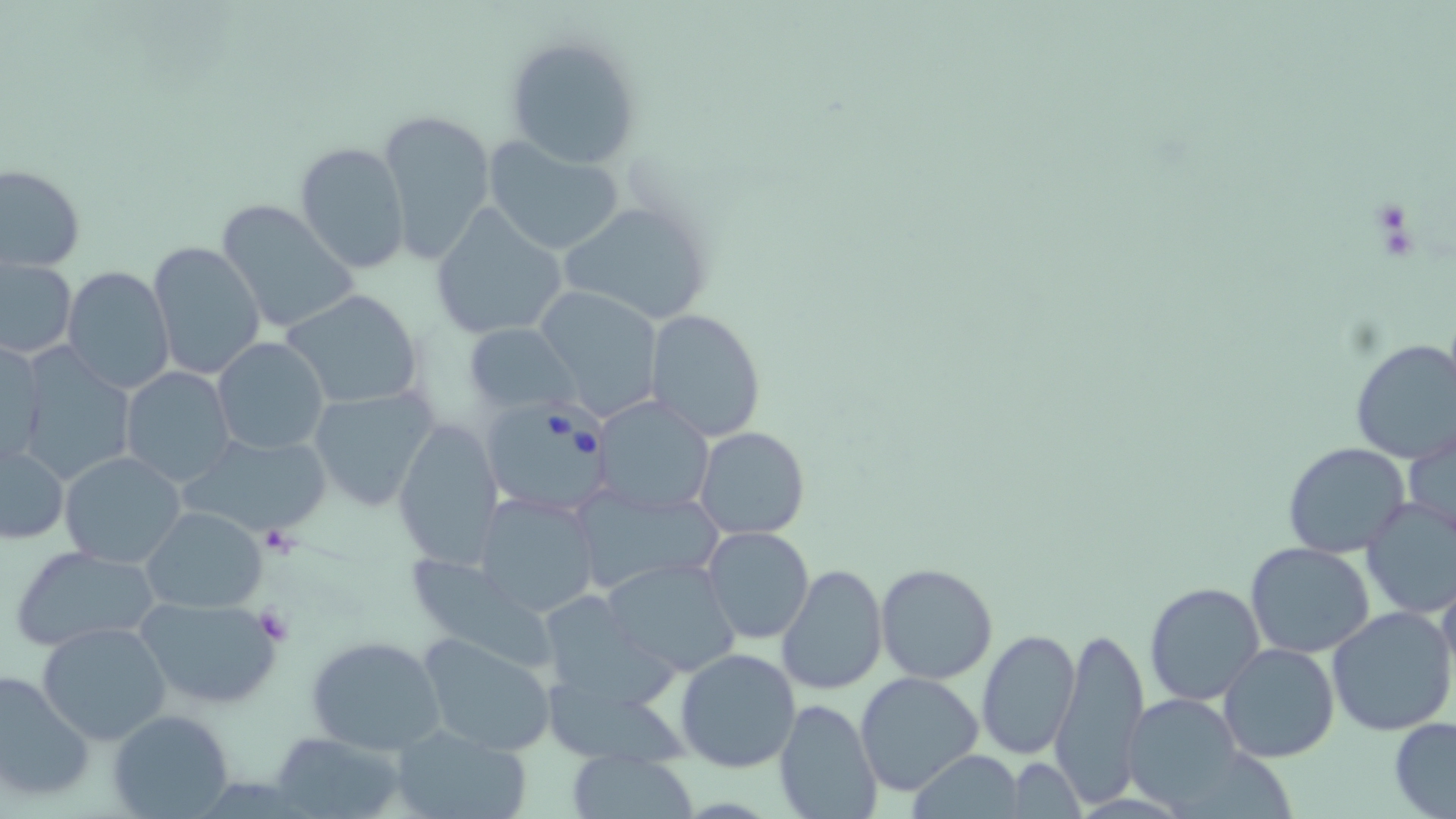 Approximate bounding boxes as (x1,y1)-(x2,y2) corner pairs in pixels. Babesia divergens-infected red blood cell locations: (481,399)-(615,514). Uninfected red blood cell locations: (502,32)-(641,171), (377,107)-(497,267), (483,136)-(626,255), (294,140)-(411,273), (1,164)-(85,272), (215,199)-(358,336), (556,200)-(714,325), (429,206)-(568,341), (148,239)-(266,380), (2,257)-(77,359), (63,266)-(174,392), (531,287)-(662,420), (283,289)-(424,409), (645,308)-(766,441), (463,323)-(579,415), (1349,337)-(1456,464), (212,338)-(330,454), (0,341)-(45,470), (14,352)-(134,486), (120,367)-(235,487), (307,385)-(437,512), (594,396)-(715,515), (393,416)-(503,567), (696,426)-(810,541), (1404,428)-(1456,544), (185,436)-(328,540), (1282,441)-(1410,558), (1,443)-(69,546), (59,451)-(187,568), (569,485)-(721,595), (472,492)-(601,618), (1358,496)-(1456,621), (141,506)-(267,613), (701,527)-(814,644), (1245,542)-(1375,659), (10,544)-(161,651), (413,555)-(557,672), (601,557)-(744,677), (876,562)-(998,684), (775,563)-(887,696), (1435,575)-(1456,703), (1143,581)-(1266,705), (133,592)-(281,712), (548,597)-(684,711), (1326,605)-(1456,738), (35,621)-(173,746), (1052,624)-(1150,805), (975,629)-(1080,758), (417,632)-(558,756), (306,635)-(446,756), (1219,644)-(1340,764), (675,647)-(801,772), (0,667)-(95,805), (856,671)-(985,795), (1124,694)-(1244,811), (773,698)-(884,819), (108,709)-(234,817), (1389,717)-(1456,817), (392,724)-(528,819), (269,731)-(407,819), (566,750)-(701,818), (909,750)-(1024,818), (1004,759)-(1084,816). Platelet locations: (256,527)-(302,556), (253,605)-(292,644). Slide-level diagnosis: Babesia divergens. Image is 1456×819 pixels. Thin blood film. Single field of view. Captured at 1000x magnification. May-Grünwald-Giemsa stain. Optical microscopy.